Locate every blood parasite and identify its species.
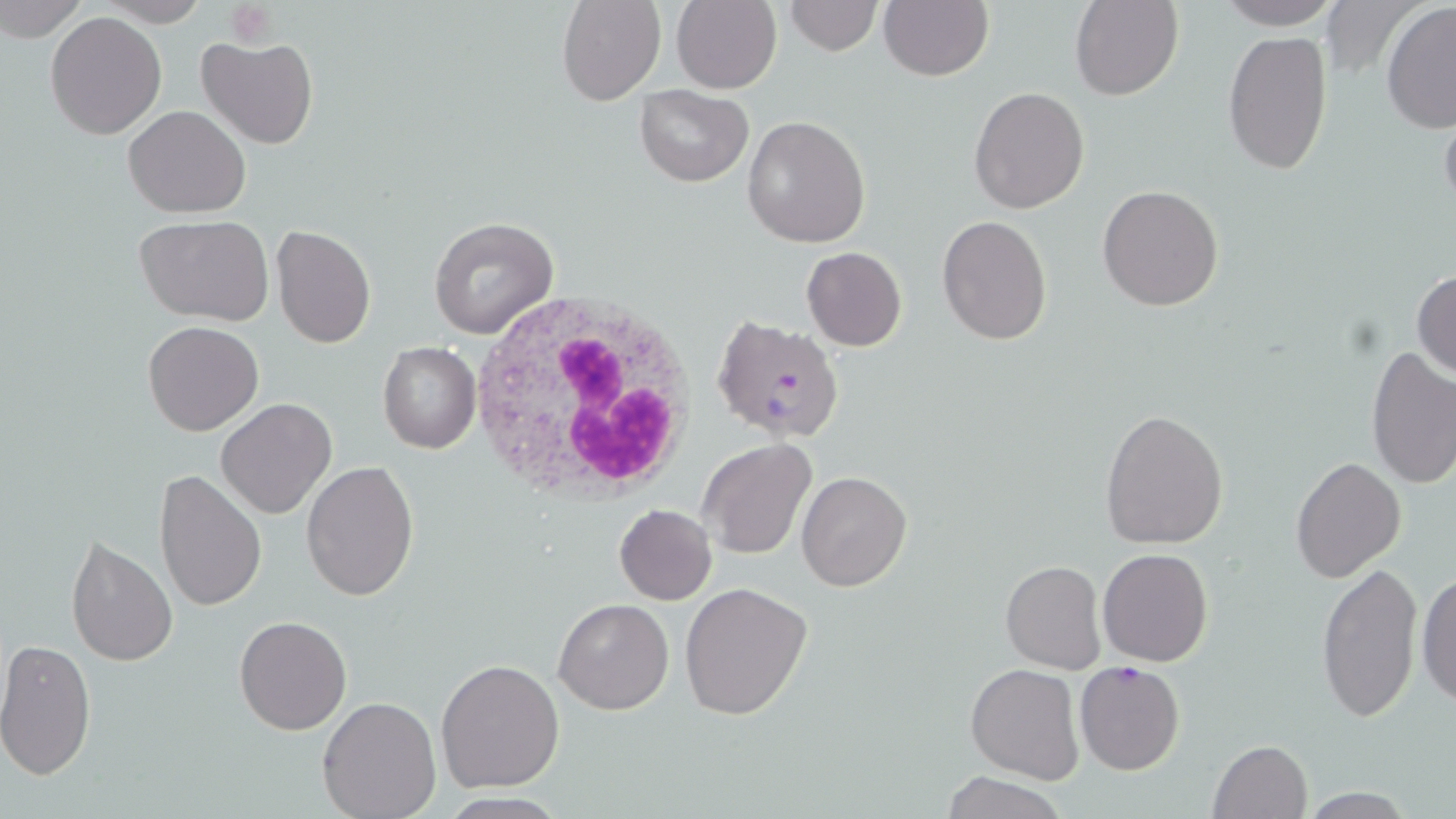

Approximate bounding boxes as named x1/y1/x2/y2 corners in pixels.
Plasmodium falciparum-infected red blood cells: (x1=712, y1=321, x2=843, y2=446), (x1=1073, y1=660, x2=1186, y2=775).
No Plasmodium ovale, Plasmodium malariae, Plasmodium vivax, Babesia divergens, or Trypanosoma brucei observed.

{
  "slide_level_diagnosis": "Plasmodium falciparum",
  "preparation": "thin blood film",
  "magnification": "1000x",
  "platelet_locations": "approximate bounding boxes as named x1/y1/x2/y2 corners in pixels: (x1=228, y1=5, x2=276, y2=44)",
  "white_blood_cell_locations": "approximate bounding boxes as named x1/y1/x2/y2 corners in pixels: (x1=466, y1=293, x2=703, y2=502)",
  "uninfected_red_blood_cell_locations": "approximate bounding boxes as named x1/y1/x2/y2 corners in pixels: (x1=0, y1=0, x2=86, y2=44), (x1=557, y1=0, x2=665, y2=105), (x1=782, y1=0, x2=883, y2=55), (x1=1070, y1=0, x2=1182, y2=101), (x1=1213, y1=0, x2=1346, y2=30), (x1=671, y1=1, x2=781, y2=92), (x1=879, y1=1, x2=992, y2=81), (x1=1380, y1=4, x2=1456, y2=133), (x1=45, y1=11, x2=167, y2=140), (x1=1222, y1=30, x2=1333, y2=178), (x1=197, y1=34, x2=318, y2=151), (x1=634, y1=86, x2=753, y2=187), (x1=968, y1=86, x2=1090, y2=214), (x1=1440, y1=101, x2=1456, y2=222), (x1=123, y1=104, x2=252, y2=217), (x1=742, y1=115, x2=872, y2=250), (x1=1097, y1=184, x2=1224, y2=311), (x1=137, y1=215, x2=274, y2=326), (x1=428, y1=215, x2=559, y2=340), (x1=937, y1=215, x2=1052, y2=343), (x1=271, y1=224, x2=376, y2=349), (x1=801, y1=247, x2=908, y2=350), (x1=1412, y1=268, x2=1456, y2=381), (x1=143, y1=319, x2=264, y2=436), (x1=377, y1=340, x2=482, y2=454), (x1=1364, y1=347, x2=1456, y2=490), (x1=216, y1=398, x2=337, y2=519), (x1=1098, y1=409, x2=1228, y2=550), (x1=698, y1=438, x2=816, y2=560), (x1=1289, y1=456, x2=1406, y2=583), (x1=300, y1=459, x2=418, y2=601), (x1=153, y1=470, x2=267, y2=614), (x1=795, y1=470, x2=913, y2=592), (x1=614, y1=505, x2=717, y2=605), (x1=67, y1=536, x2=177, y2=667), (x1=1097, y1=548, x2=1213, y2=666), (x1=999, y1=560, x2=1106, y2=675), (x1=1316, y1=561, x2=1422, y2=724), (x1=1416, y1=567, x2=1455, y2=708), (x1=680, y1=581, x2=812, y2=722), (x1=552, y1=598, x2=674, y2=715), (x1=234, y1=615, x2=350, y2=735), (x1=0, y1=638, x2=97, y2=780), (x1=435, y1=658, x2=566, y2=793), (x1=966, y1=664, x2=1082, y2=784), (x1=318, y1=695, x2=442, y2=819), (x1=1207, y1=738, x2=1313, y2=819), (x1=940, y1=771, x2=1068, y2=819)",
  "stain": "May-Grünwald-Giemsa",
  "modality": "light microscopy",
  "image_size": "1456×819 pixels",
  "field_of_view": "one of a larger specimen"
}